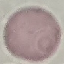

malaria status = uninfected
preparation = thin blood film
capture = smartphone through the microscope eyepiece
stain = Giemsa
image type = automatically extracted cell patch, resized to 64 × 64 pixels